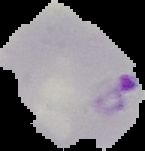

Summary:
  - Preparation: thin blood film
  - Image type: cell region segmented out of the field of view; surrounding area masked to black
  - Result: Plasmodium parasites detected
  - Image size: 145×151 pixels